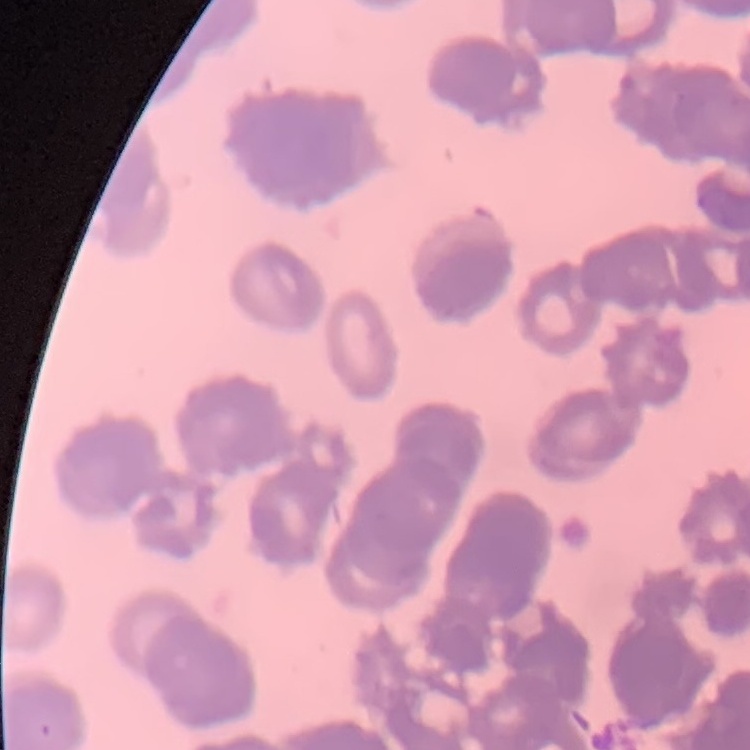
red blood cell morphology = rouleaux formation
preparation = thin blood film
image type = square crop of a larger photomicrograph
stain = Field's or Giemsa